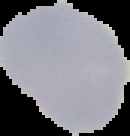

image_type: segmented cell region on a black background
preparation: thin blood smear
image_size: 130×136 pixels
result: no Plasmodium parasites detected